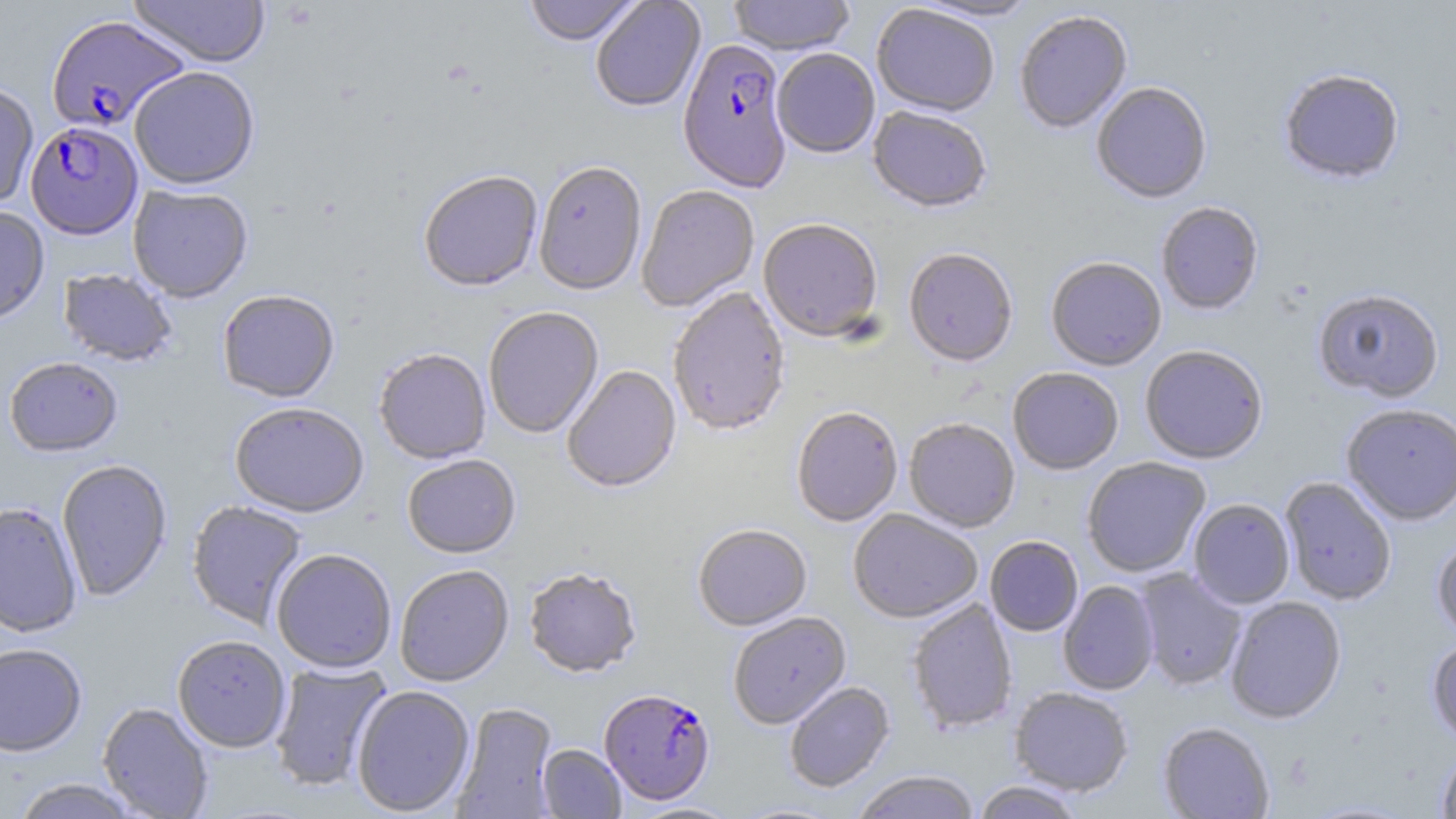

Summary:
  - Coordinate format: approximate bounding boxes as named x1/y1/x2/y2 corners in pixels
  - Plasmodium falciparum-infected red blood cell locations: (x1=46, y1=17, x2=190, y2=134), (x1=678, y1=41, x2=792, y2=196), (x1=26, y1=124, x2=143, y2=242), (x1=599, y1=690, x2=715, y2=806)
  - Uninfected red blood cell locations: (x1=127, y1=0, x2=269, y2=70), (x1=523, y1=0, x2=642, y2=48), (x1=591, y1=0, x2=706, y2=114), (x1=728, y1=0, x2=855, y2=59), (x1=909, y1=0, x2=1042, y2=24), (x1=871, y1=6, x2=998, y2=119), (x1=1014, y1=13, x2=1133, y2=135), (x1=772, y1=51, x2=880, y2=160), (x1=130, y1=69, x2=260, y2=192), (x1=1278, y1=71, x2=1405, y2=186), (x1=0, y1=82, x2=39, y2=210), (x1=1092, y1=84, x2=1212, y2=205), (x1=868, y1=108, x2=990, y2=215), (x1=534, y1=163, x2=647, y2=298), (x1=419, y1=172, x2=543, y2=294), (x1=128, y1=186, x2=253, y2=305), (x1=636, y1=186, x2=760, y2=313), (x1=1156, y1=203, x2=1264, y2=316), (x1=0, y1=207, x2=50, y2=327), (x1=758, y1=220, x2=883, y2=344), (x1=903, y1=250, x2=1018, y2=369), (x1=1045, y1=259, x2=1166, y2=372), (x1=58, y1=269, x2=177, y2=368), (x1=668, y1=289, x2=790, y2=438), (x1=218, y1=291, x2=340, y2=405), (x1=1313, y1=291, x2=1445, y2=404), (x1=484, y1=308, x2=604, y2=439), (x1=1140, y1=347, x2=1268, y2=466), (x1=374, y1=350, x2=491, y2=465), (x1=5, y1=359, x2=122, y2=459), (x1=563, y1=367, x2=682, y2=495), (x1=1008, y1=369, x2=1124, y2=477), (x1=229, y1=404, x2=369, y2=519), (x1=1341, y1=405, x2=1456, y2=526), (x1=791, y1=408, x2=903, y2=528), (x1=904, y1=420, x2=1020, y2=533), (x1=403, y1=455, x2=521, y2=560), (x1=1082, y1=458, x2=1210, y2=578), (x1=57, y1=461, x2=172, y2=602), (x1=1279, y1=477, x2=1396, y2=606), (x1=1188, y1=499, x2=1295, y2=609), (x1=187, y1=501, x2=307, y2=631), (x1=0, y1=503, x2=82, y2=638), (x1=848, y1=510, x2=982, y2=624), (x1=693, y1=525, x2=812, y2=632), (x1=1432, y1=536, x2=1456, y2=643), (x1=985, y1=537, x2=1083, y2=637), (x1=271, y1=550, x2=397, y2=674), (x1=395, y1=566, x2=514, y2=688), (x1=524, y1=569, x2=642, y2=680), (x1=1135, y1=569, x2=1247, y2=690), (x1=1058, y1=581, x2=1159, y2=696), (x1=1225, y1=598, x2=1346, y2=724), (x1=907, y1=600, x2=1018, y2=734), (x1=728, y1=612, x2=851, y2=730), (x1=172, y1=637, x2=290, y2=753), (x1=1426, y1=639, x2=1456, y2=748), (x1=0, y1=645, x2=87, y2=759), (x1=268, y1=660, x2=393, y2=792), (x1=784, y1=681, x2=895, y2=793), (x1=351, y1=686, x2=476, y2=817), (x1=1010, y1=687, x2=1133, y2=797), (x1=98, y1=703, x2=214, y2=818), (x1=450, y1=703, x2=559, y2=818), (x1=1158, y1=722, x2=1274, y2=819), (x1=537, y1=745, x2=626, y2=818), (x1=1436, y1=749, x2=1456, y2=819), (x1=851, y1=771, x2=981, y2=819), (x1=12, y1=779, x2=142, y2=819), (x1=971, y1=781, x2=1086, y2=819), (x1=1299, y1=799, x2=1421, y2=818), (x1=629, y1=801, x2=742, y2=819), (x1=731, y1=801, x2=845, y2=818)
  - Slide-level diagnosis: Plasmodium falciparum
  - Field of view: one of a larger specimen
  - Image size: 1456×819 pixels
  - Preparation: thin blood smear
  - Stain: May-Grünwald-Giemsa
  - Magnification: 1000x
  - Modality: optical microscopy